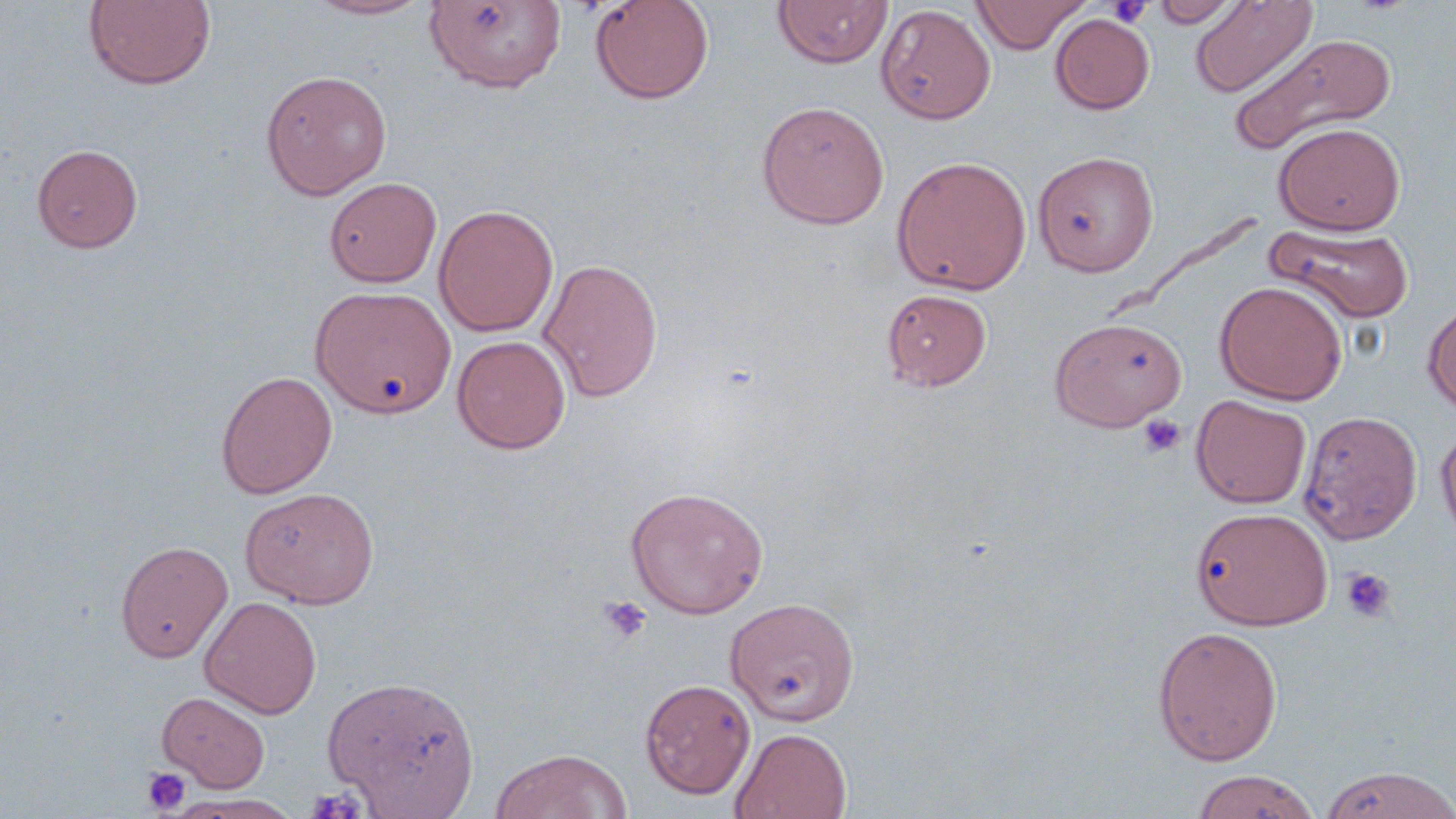

slide_level_diagnosis: negative for blood parasites
platelet_locations: 'approximate bounding boxes as (x1, y1, x2, y2) in pixels: (1107, 1, 1153, 28), (1138, 414, 1186, 458), (1340, 567, 1396, 622), (599, 595, 653, 643), (141, 767, 191, 815), (305, 785, 367, 819)'
uninfected_red_blood_cell_locations: 'approximate bounding boxes as (x1, y1, x2, y2) in pixels: (83, 0, 217, 91), (303, 0, 435, 20), (589, 0, 714, 104), (772, 0, 892, 69), (971, 0, 1091, 54), (1152, 0, 1243, 27), (1190, 0, 1317, 98), (426, 1, 565, 92), (876, 4, 996, 125), (1050, 14, 1155, 114), (1228, 33, 1396, 154), (260, 70, 392, 199), (756, 100, 890, 229), (1274, 122, 1405, 235), (31, 143, 143, 253), (1032, 151, 1159, 277), (892, 155, 1031, 295), (324, 177, 442, 288), (433, 204, 559, 337), (1265, 223, 1414, 324), (538, 257, 664, 402), (1214, 280, 1348, 405), (310, 285, 456, 419), (882, 288, 992, 391), (1422, 299, 1456, 417), (1049, 316, 1188, 431), (452, 335, 571, 454), (215, 370, 337, 498), (1191, 395, 1311, 508), (1298, 410, 1422, 545), (1436, 423, 1456, 551), (625, 485, 769, 619), (240, 486, 379, 609), (1190, 506, 1333, 630), (116, 540, 232, 662), (200, 596, 321, 718), (725, 597, 861, 726), (1152, 625, 1283, 766), (322, 674, 480, 816), (640, 678, 756, 800), (158, 690, 270, 792), (730, 727, 852, 818), (489, 748, 633, 819), (1317, 766, 1456, 819), (1191, 770, 1320, 819), (167, 794, 303, 818)'
stain: May-Grünwald-Giemsa
field_of_view: single
magnification: 1000x
image_size: 1456×819 pixels
preparation: thin blood smear
modality: light microscopy